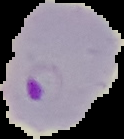

preparation = thin blood smear
result = malaria parasites detected
image type = segmented cell region on a black background
image size = 124×139 pixels